Classify this cell by malaria status.
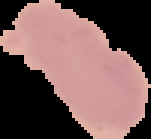

Uninfected.

From a thin blood smear. Segmented cell region on a black background. Image is 151×139 pixels.